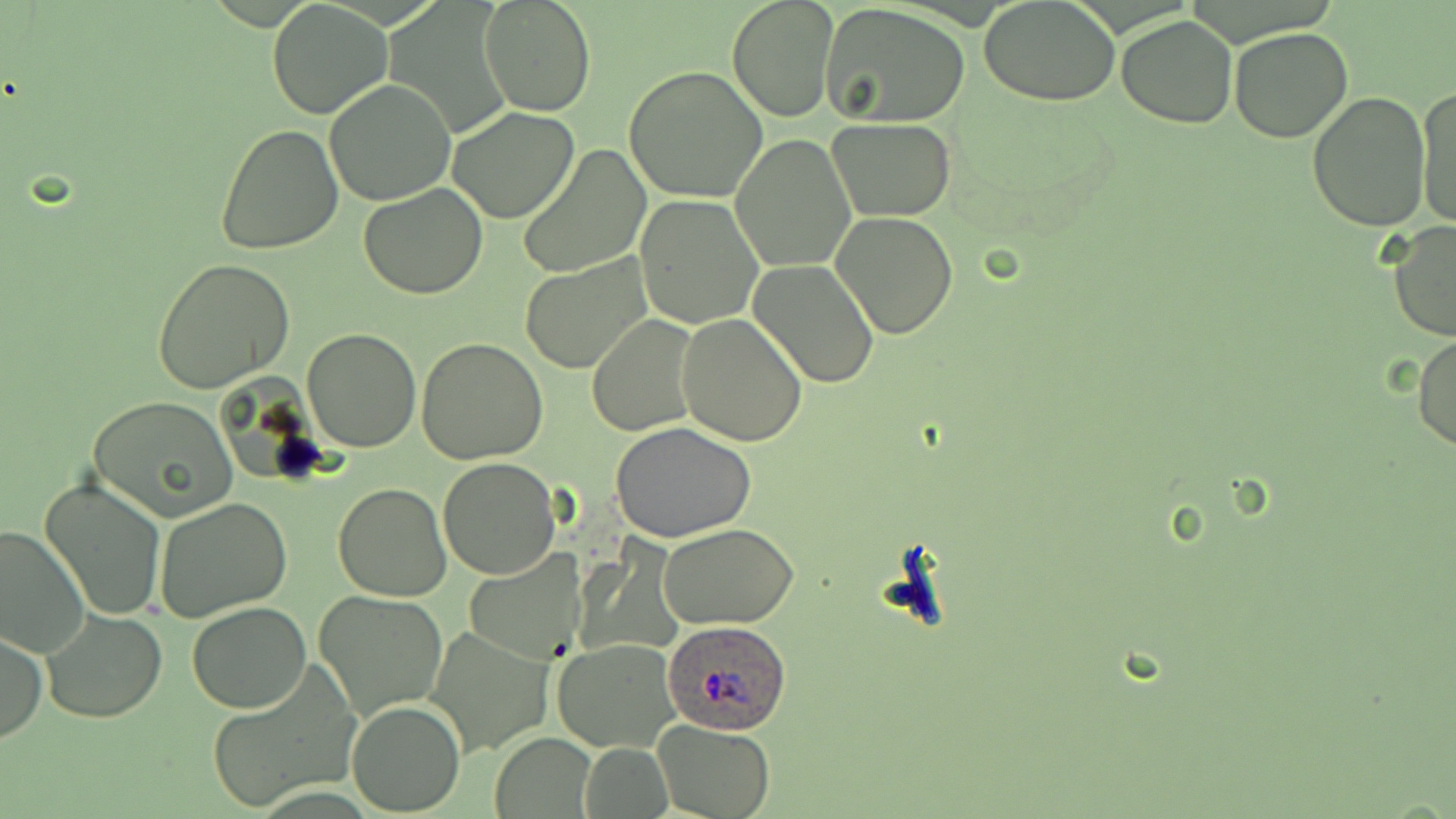

Summary:
  - Coordinate format: approximate bounding boxes as [x1, y1, x2, y2] in pixels
  - Plasmodium ovale-infected red blood cell locations: [661, 618, 794, 733]
  - Uninfected red blood cell locations: [480, 0, 596, 116], [726, 0, 839, 122], [979, 0, 1121, 108], [266, 1, 391, 119], [820, 3, 970, 128], [1116, 14, 1238, 129], [1228, 26, 1355, 144], [623, 65, 768, 202], [324, 79, 457, 206], [1414, 84, 1455, 234], [1307, 91, 1433, 231], [447, 107, 581, 223], [826, 117, 957, 220], [215, 122, 345, 256], [731, 134, 857, 272], [518, 145, 651, 278], [357, 183, 488, 299], [634, 193, 764, 329], [830, 211, 960, 340], [1385, 219, 1456, 343], [518, 257, 650, 374], [152, 258, 297, 395], [749, 259, 880, 387], [677, 312, 807, 447], [588, 316, 701, 437], [302, 327, 422, 452], [1412, 331, 1456, 454], [416, 338, 549, 464], [86, 396, 238, 522], [610, 421, 756, 543], [438, 457, 560, 580], [39, 476, 168, 621], [333, 483, 453, 601], [154, 497, 292, 624], [658, 523, 799, 630], [0, 524, 90, 662], [463, 550, 589, 663], [314, 588, 450, 722], [186, 602, 311, 713], [41, 609, 167, 724], [426, 624, 557, 757], [1, 629, 47, 745], [551, 639, 677, 752], [203, 664, 359, 813], [346, 698, 464, 815], [653, 719, 775, 818], [492, 733, 596, 817], [576, 742, 674, 819]
  - Slide-level diagnosis: Plasmodium ovale
  - Magnification: 1000x
  - Modality: optical microscopy
  - Image size: 1456×819 pixels
  - Field of view: single
  - Preparation: thin blood film
  - Stain: May-Grünwald-Giemsa